Describe the morphology of the red blood cells.
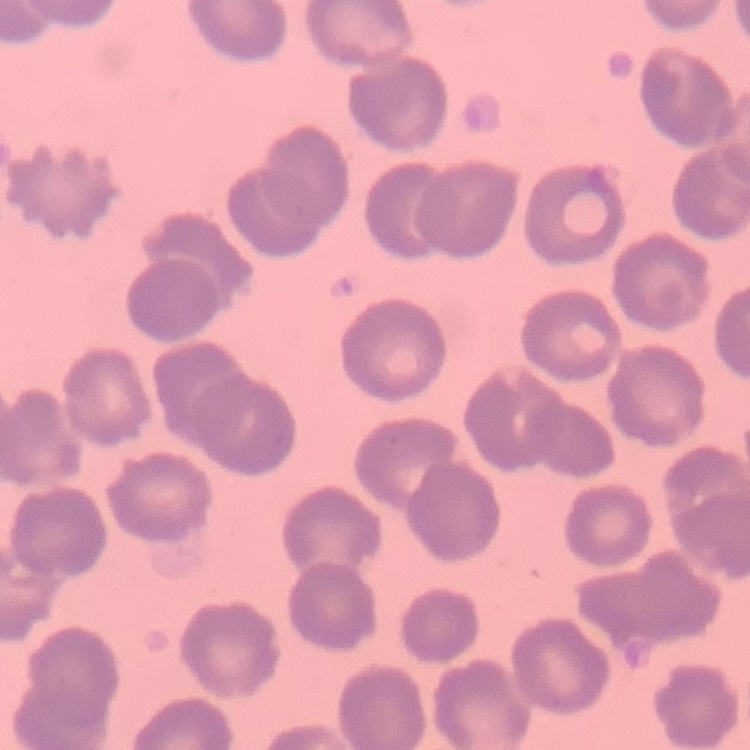
No rouleaux formation.

{
  "preparation": "thin blood film",
  "stain": "Field's or Giemsa",
  "image_type": "square crop of a larger photomicrograph"
}